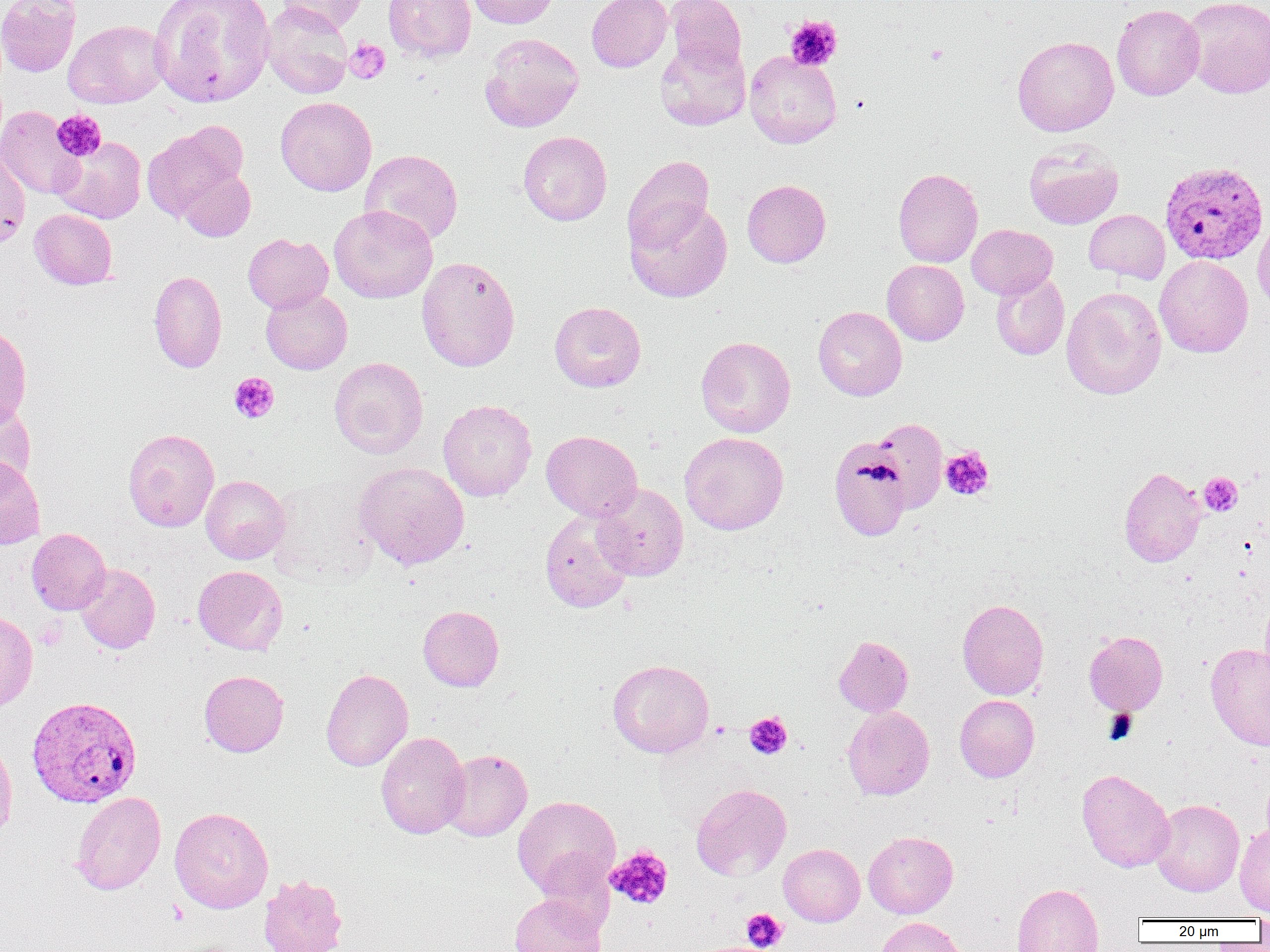

slide-level diagnosis = Plasmodium vivax
preparation = thin blood smear
field of view = single
uninfected red blood cell locations (subset) = approximate bounding boxes as named x1/y1/x2/y2 corners in pixels: (x1=0, y1=0, x2=81, y2=77), (x1=149, y1=0, x2=275, y2=107), (x1=276, y1=0, x2=368, y2=34), (x1=383, y1=0, x2=476, y2=62), (x1=467, y1=0, x2=561, y2=28), (x1=586, y1=0, x2=672, y2=72), (x1=665, y1=0, x2=746, y2=74), (x1=1182, y1=0, x2=1269, y2=98), (x1=261, y1=2, x2=353, y2=99), (x1=1112, y1=4, x2=1205, y2=101), (x1=64, y1=20, x2=168, y2=109), (x1=479, y1=32, x2=584, y2=133), (x1=1012, y1=35, x2=1119, y2=136), (x1=655, y1=40, x2=750, y2=131), (x1=744, y1=51, x2=842, y2=148), (x1=275, y1=96, x2=377, y2=196), (x1=0, y1=106, x2=84, y2=199), (x1=142, y1=123, x2=246, y2=222), (x1=518, y1=130, x2=612, y2=226), (x1=53, y1=136, x2=146, y2=224), (x1=1024, y1=143, x2=1123, y2=229), (x1=0, y1=144, x2=30, y2=249), (x1=360, y1=149, x2=463, y2=245), (x1=623, y1=155, x2=714, y2=252), (x1=175, y1=165, x2=256, y2=241), (x1=893, y1=168, x2=983, y2=267), (x1=742, y1=179, x2=831, y2=267), (x1=625, y1=198, x2=732, y2=302), (x1=329, y1=205, x2=438, y2=303), (x1=29, y1=208, x2=117, y2=289), (x1=1084, y1=209, x2=1170, y2=284), (x1=1252, y1=217, x2=1270, y2=316), (x1=966, y1=224, x2=1057, y2=300), (x1=243, y1=233, x2=333, y2=313), (x1=1155, y1=255, x2=1253, y2=358), (x1=416, y1=256, x2=520, y2=372), (x1=882, y1=260, x2=969, y2=345), (x1=149, y1=270, x2=227, y2=373), (x1=991, y1=270, x2=1070, y2=360), (x1=1061, y1=286, x2=1166, y2=400), (x1=260, y1=289, x2=352, y2=375), (x1=549, y1=301, x2=646, y2=392), (x1=813, y1=306, x2=907, y2=401), (x1=0, y1=324, x2=32, y2=426), (x1=695, y1=336, x2=795, y2=437), (x1=328, y1=356, x2=428, y2=459), (x1=0, y1=396, x2=36, y2=492), (x1=438, y1=399, x2=537, y2=502), (x1=869, y1=419, x2=948, y2=514), (x1=123, y1=428, x2=219, y2=531), (x1=541, y1=430, x2=642, y2=521), (x1=679, y1=431, x2=789, y2=535), (x1=827, y1=437, x2=912, y2=543), (x1=0, y1=456, x2=45, y2=550), (x1=353, y1=462, x2=470, y2=570), (x1=1119, y1=467, x2=1206, y2=567), (x1=201, y1=475, x2=290, y2=564), (x1=267, y1=475, x2=379, y2=585), (x1=591, y1=483, x2=689, y2=581), (x1=540, y1=510, x2=634, y2=613), (x1=26, y1=528, x2=111, y2=615), (x1=74, y1=562, x2=160, y2=654), (x1=193, y1=565, x2=288, y2=655), (x1=1259, y1=593, x2=1270, y2=685), (x1=957, y1=599, x2=1048, y2=700), (x1=418, y1=605, x2=504, y2=692), (x1=0, y1=611, x2=38, y2=714), (x1=1084, y1=631, x2=1168, y2=715), (x1=834, y1=636, x2=913, y2=717), (x1=1206, y1=643, x2=1270, y2=750), (x1=607, y1=659, x2=714, y2=758), (x1=321, y1=668, x2=413, y2=771), (x1=199, y1=670, x2=289, y2=757), (x1=954, y1=694, x2=1039, y2=782), (x1=843, y1=706, x2=935, y2=800), (x1=376, y1=731, x2=470, y2=839), (x1=0, y1=733, x2=17, y2=846), (x1=439, y1=748, x2=532, y2=841), (x1=1077, y1=768, x2=1175, y2=872), (x1=691, y1=783, x2=791, y2=881), (x1=70, y1=791, x2=166, y2=895), (x1=512, y1=795, x2=620, y2=899), (x1=1151, y1=799, x2=1244, y2=896), (x1=169, y1=807, x2=273, y2=913), (x1=1235, y1=824, x2=1270, y2=916), (x1=863, y1=831, x2=958, y2=918), (x1=778, y1=843, x2=865, y2=926), (x1=258, y1=874, x2=347, y2=952), (x1=1012, y1=883, x2=1104, y2=952), (x1=510, y1=893, x2=607, y2=952), (x1=874, y1=917, x2=968, y2=952)
magnification = 1000x
Plasmodium vivax-infected red blood cell locations (subset) = approximate bounding boxes as named x1/y1/x2/y2 corners in pixels: (x1=1160, y1=161, x2=1268, y2=265)
image size = 1270×952 pixels
modality = light microscopy
platelet locations = approximate bounding boxes as named x1/y1/x2/y2 corners in pixels: (x1=784, y1=16, x2=843, y2=70), (x1=344, y1=39, x2=390, y2=84), (x1=925, y1=43, x2=949, y2=66), (x1=51, y1=110, x2=106, y2=162), (x1=229, y1=372, x2=279, y2=424), (x1=940, y1=446, x2=995, y2=500), (x1=1199, y1=472, x2=1242, y2=516), (x1=1105, y1=709, x2=1138, y2=743), (x1=744, y1=712, x2=793, y2=760), (x1=605, y1=845, x2=673, y2=910), (x1=741, y1=908, x2=787, y2=951)